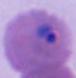
magnification = 400x or 1000x
modality = photomicrograph
identification = Plasmodium